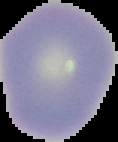

image_type: segmented cell region on a black background
preparation: thin blood smear
result: no malaria parasites seen
image_size: 118×142 pixels